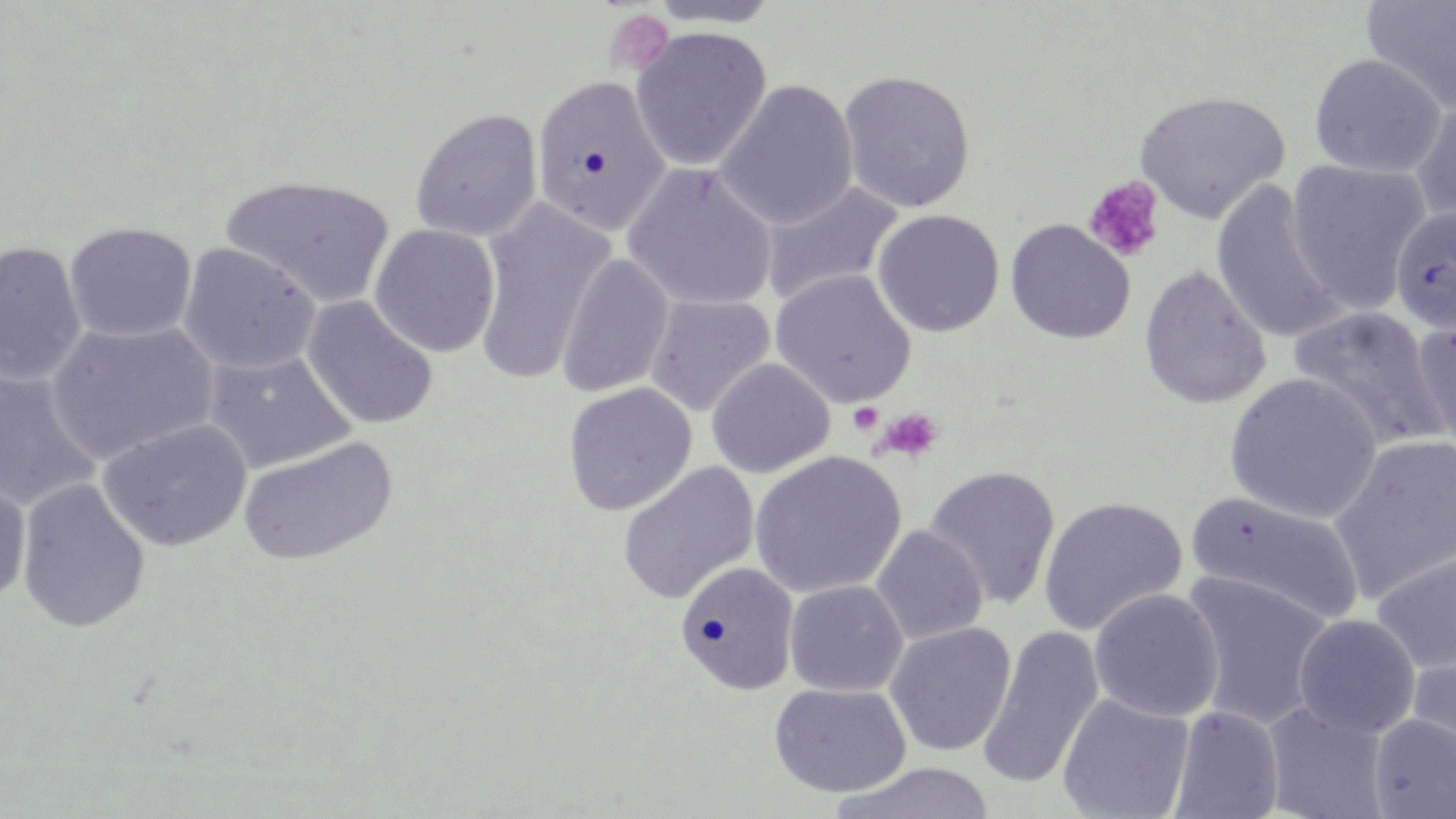 Approximate bounding boxes as (x1,y1)-(x2,y2) corner pairs in pixels. Platelet locations (subset): (603,8)-(674,77), (1084,176)-(1165,262), (849,402)-(883,435), (873,407)-(945,463). Uninfected red blood cell locations (subset): (645,0)-(782,29), (1360,1)-(1456,115), (630,26)-(772,171), (1309,53)-(1446,178), (837,69)-(977,214), (531,75)-(671,239), (714,80)-(858,231), (1133,90)-(1290,223), (1409,97)-(1456,228), (409,107)-(543,242), (1285,159)-(1432,314), (622,162)-(778,312), (220,175)-(396,308), (759,180)-(904,309), (1209,181)-(1345,344), (473,198)-(616,385), (1389,206)-(1456,336), (871,208)-(1005,337), (1004,219)-(1136,344), (63,221)-(197,343), (368,223)-(501,358), (0,240)-(86,387), (177,242)-(320,375), (555,253)-(674,400), (1138,263)-(1272,410), (644,294)-(776,417), (301,296)-(439,430), (1288,306)-(1446,449), (1413,318)-(1456,458), (45,320)-(218,465), (201,348)-(356,475), (705,358)-(835,479), (0,368)-(101,512), (1223,372)-(1384,523), (562,382)-(698,517), (97,418)-(251,552), (237,435)-(398,567), (1328,436)-(1456,603), (748,450)-(906,598), (616,461)-(759,605), (923,465)-(1061,610), (0,475)-(32,608), (16,478)-(151,634), (1186,491)-(1364,627), (1038,496)-(1188,636), (870,525)-(988,645), (1369,545)-(1456,675), (675,561)-(799,696), (1180,571)-(1334,730), (784,580)-(908,697), (1089,588)-(1224,722), (1293,614)-(1421,739), (884,622)-(1017,756), (975,625)-(1104,791), (1404,646)-(1456,772), (768,682)-(911,797), (1057,692)-(1195,819), (1261,702)-(1390,818), (1168,705)-(1285,819), (1369,714)-(1456,818), (831,762)-(997,819). Slide-level diagnosis: no evidence of blood parasites. May-Grünwald-Giemsa-stained preparation. Light microscopy. Thin blood film. One field of a larger specimen. Image is 1456×819 pixels. Captured at 1000x magnification.